Locate leukocytes (white blood cells).
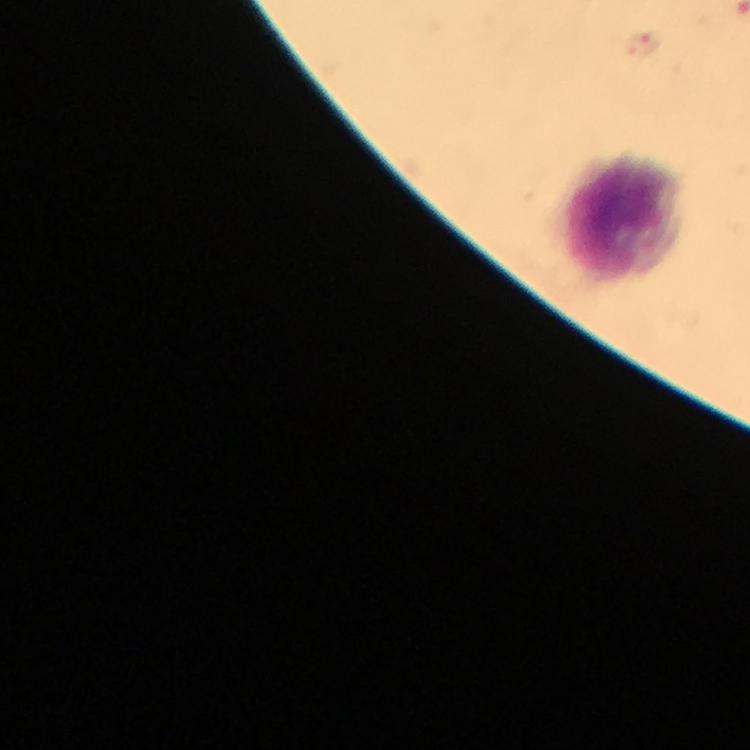

Approximate object centers, in pixels from the top-left corner.
Leukocytes: (x=624, y=220).

magnification = 100x
stain = Giemsa
image size = 750×750 pixels
cropped from = one field of view
context = from a malaria diagnostic workup
capture = smartphone mounted on the microscope
preparation = thick blood smear
Plasmodium parasite locations = approximate object centers, in pixels from the top-left corner: (x=643, y=47)
immersion oil = used